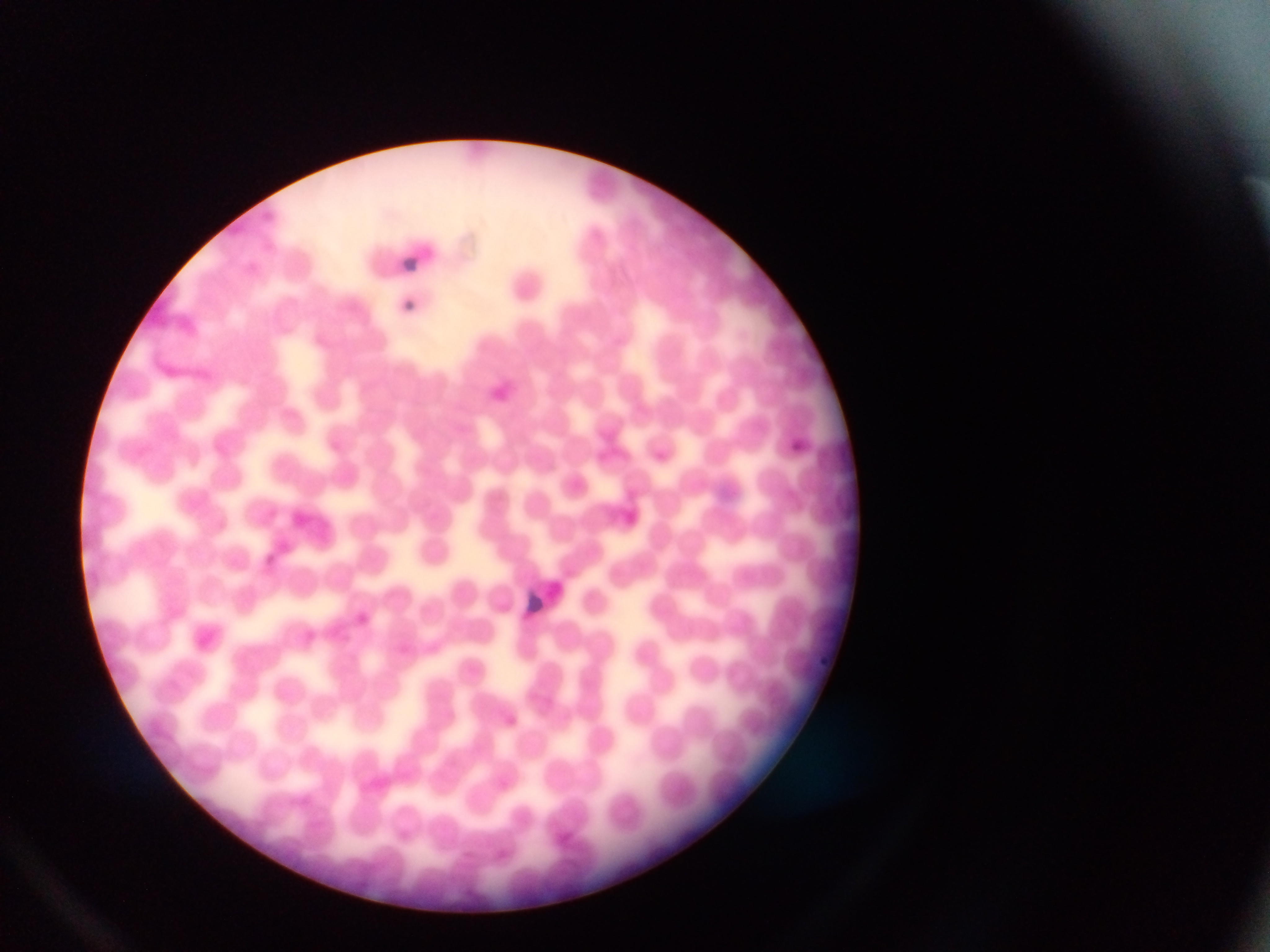
Approximate bounding boxes as (left, top, right, bottom) in pixels.
Summary:
  - Plasmodium parasite locations: (791, 440, 811, 459), (261, 553, 270, 567), (354, 611, 368, 629), (813, 654, 838, 670)
  - Leukocyte locations: (499, 258, 552, 309)
  - Capture: mobile-phone photograph through a microscope
  - Country: Ghana
  - Image size: 1270×952 pixels
  - Preparation: thin blood smear
  - Field of view: single